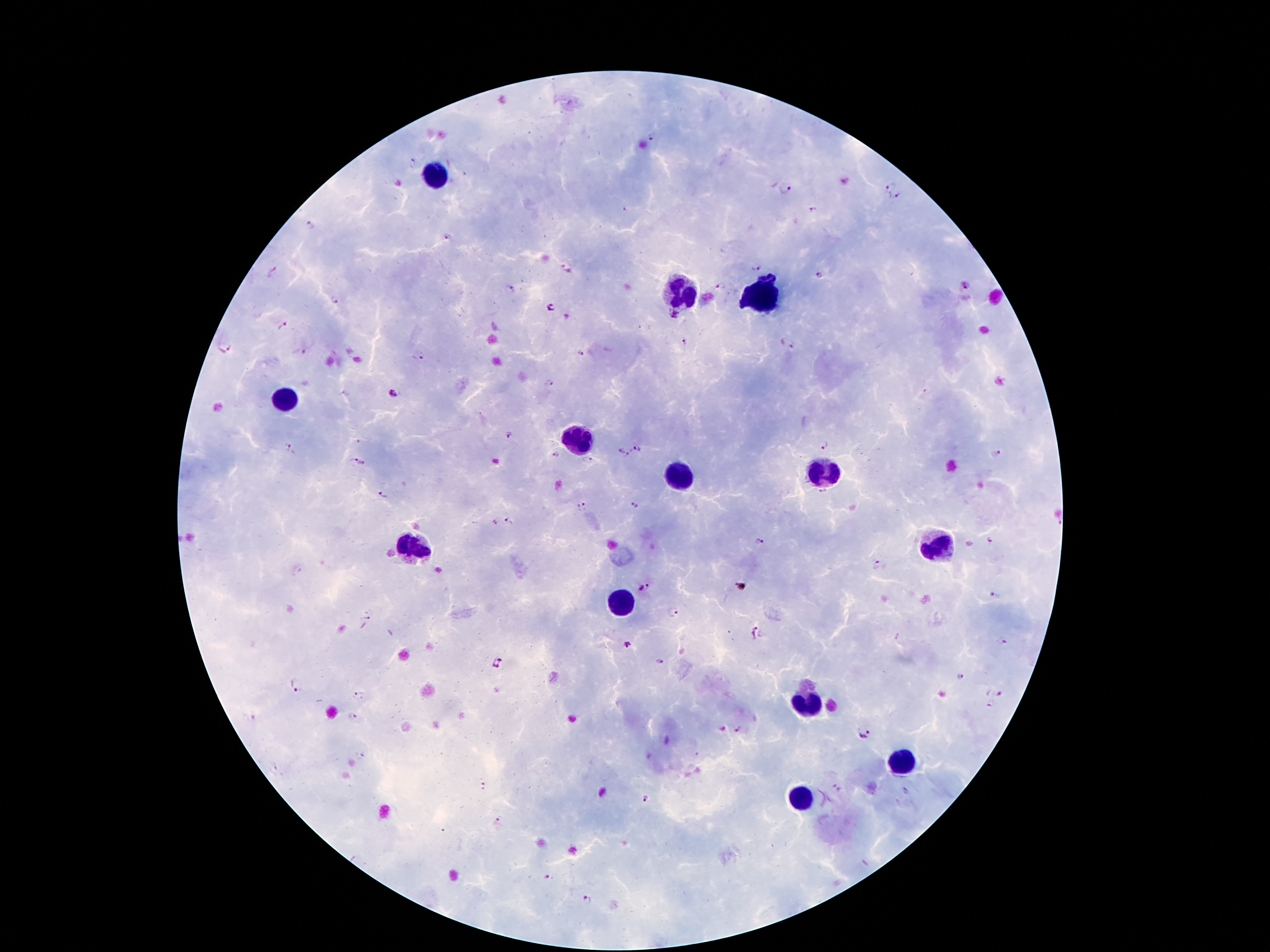

Approximate object centers, in pixels from the top-left corner.
Summary:
  - Malaria parasite locations: (x=654, y=134), (x=412, y=161), (x=786, y=188), (x=891, y=189), (x=900, y=198), (x=812, y=210), (x=310, y=226), (x=445, y=236), (x=755, y=267), (x=565, y=268), (x=274, y=271), (x=819, y=274), (x=719, y=285), (x=964, y=286), (x=511, y=288), (x=335, y=300), (x=552, y=307), (x=673, y=316), (x=283, y=327), (x=683, y=341), (x=787, y=344), (x=224, y=347), (x=580, y=354), (x=419, y=356), (x=549, y=383), (x=394, y=394), (x=509, y=436), (x=825, y=445), (x=288, y=447), (x=636, y=448), (x=619, y=451), (x=995, y=453), (x=555, y=455), (x=628, y=455), (x=588, y=459), (x=359, y=463), (x=384, y=495), (x=634, y=505), (x=580, y=506), (x=509, y=522), (x=989, y=541), (x=759, y=542), (x=876, y=565), (x=645, y=587), (x=994, y=595), (x=368, y=613), (x=672, y=613), (x=753, y=634), (x=1002, y=641), (x=628, y=646), (x=500, y=663), (x=959, y=678), (x=298, y=686), (x=1000, y=694), (x=360, y=696), (x=991, y=704), (x=352, y=717), (x=739, y=730), (x=864, y=735), (x=362, y=756), (x=484, y=787), (x=836, y=788), (x=646, y=799), (x=500, y=820), (x=551, y=878), (x=587, y=901)
  - Leukocyte locations: (x=438, y=173), (x=678, y=295), (x=760, y=299), (x=282, y=397), (x=576, y=442), (x=822, y=471), (x=678, y=480), (x=938, y=543), (x=414, y=549), (x=622, y=605), (x=804, y=705), (x=900, y=762), (x=802, y=800)
  - Patient malaria status: positive for Plasmodium falciparum
  - Image size: 1270×952 pixels
  - Preparation: thick peripheral-blood smear
  - Stain: Giemsa
  - Field of view: single
  - Capture: smartphone camera through the microscope eyepiece
  - Magnification: 100x